Identify the blood parasite species.
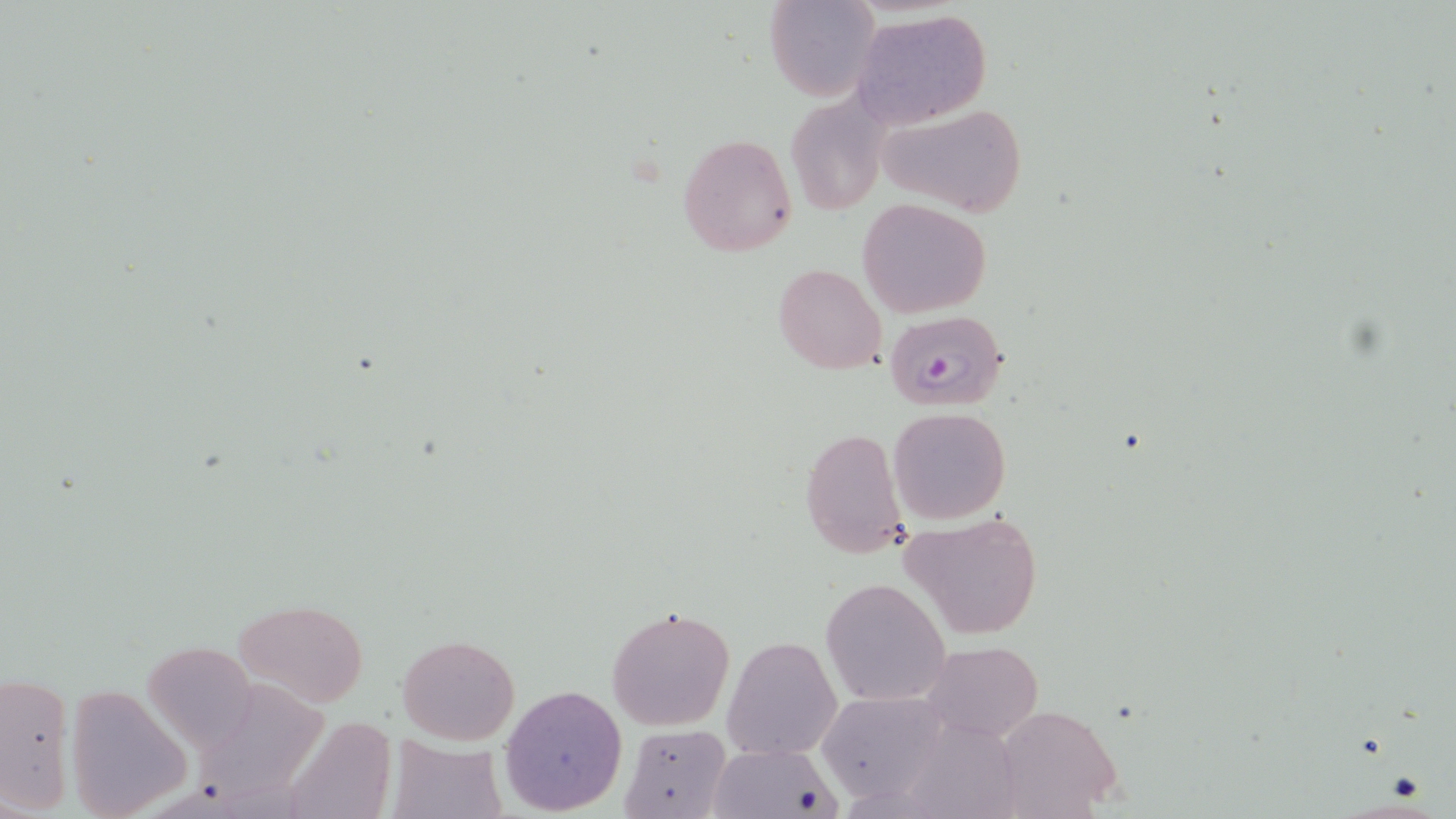

Plasmodium falciparum.

Approximate bounding boxes as (x1, y1, x2, y2) in pixels. Uninfected red blood cell locations: (764, 1, 880, 102), (852, 10, 992, 129), (787, 92, 888, 216), (874, 103, 1028, 218), (677, 131, 797, 257), (859, 199, 990, 317), (774, 262, 887, 374), (887, 406, 1011, 525), (799, 425, 909, 560), (899, 510, 1044, 640), (820, 578, 950, 706), (238, 599, 368, 707), (607, 606, 735, 731), (398, 634, 520, 746), (723, 635, 842, 760), (922, 640, 1041, 744), (145, 641, 256, 751), (0, 673, 73, 813), (500, 682, 628, 816), (66, 687, 191, 819), (817, 691, 950, 804), (987, 701, 1126, 819), (281, 718, 396, 819), (618, 724, 732, 819), (384, 737, 508, 819), (708, 742, 840, 819). Platelet locations: (1385, 772, 1426, 803). Plasmodium falciparum-infected red blood cell locations: (883, 309, 1007, 411). Optical microscopy. 1000x magnification. Image is 1456×819 pixels. May-Grünwald-Giemsa-stained preparation. Thin blood film. One field of a larger specimen.